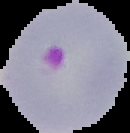
Cell region segmented out of the field of view; the surrounding area is masked to black. From a thin blood film. Malaria status: parasitized. Image is 130×133 pixels.